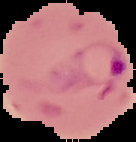
preparation: thin blood smear
image_size: 136×142 pixels
image_type: segmented cell region on a black background
malaria_status: parasitized